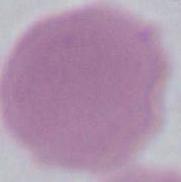
{
  "identification": "erythrocyte",
  "magnification": "1000x",
  "modality": "photomicrograph"
}